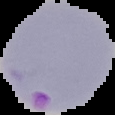
Segmented cell region on a black background. Image is 115×115 pixels. From a thin blood film. Malaria status: parasitized.